Assess this cell for malaria.
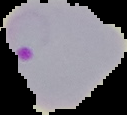
It is parasitized.

{
  "preparation": "thin blood film",
  "image_type": "cell region segmented out of the field of view; surrounding area masked to black",
  "image_size": "127×115 pixels"
}